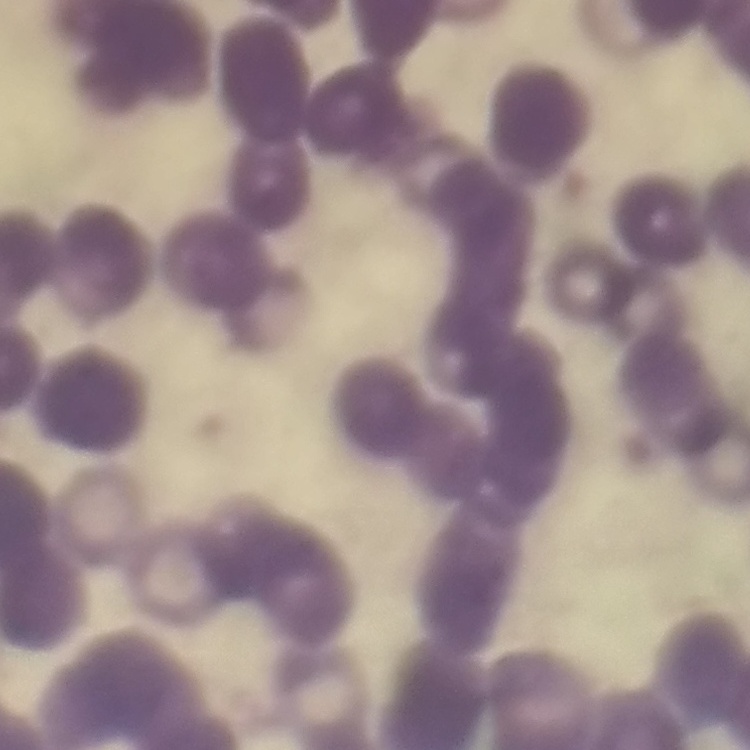

The red blood cells exhibit rouleaux formation. Thin blood smear. Stained with either Field's or Giemsa. Square crop of a larger photomicrograph.